Describe the morphology of the erythrocytes.
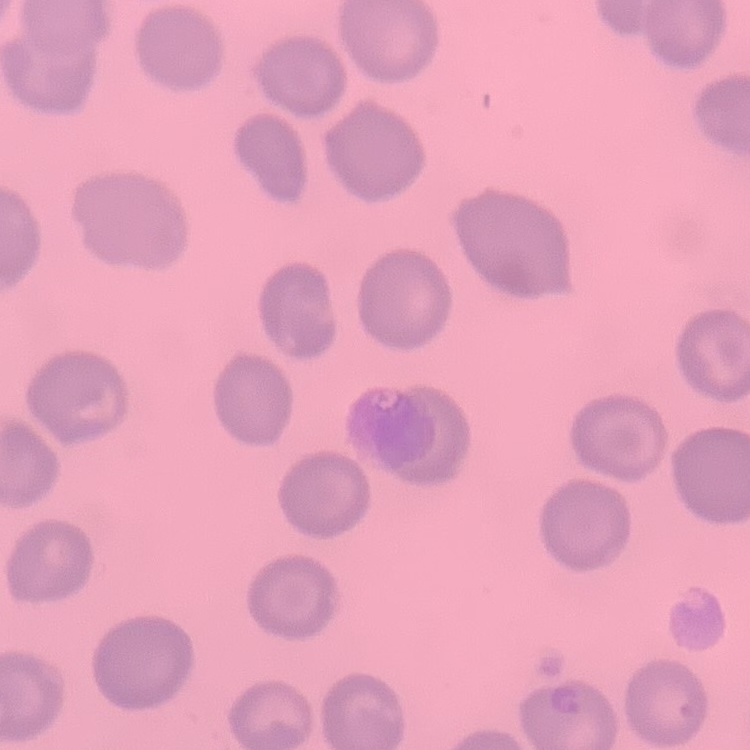

No rouleaux formation.

{
  "image_type": "square crop of a larger photomicrograph",
  "stain": "Field's or Giemsa",
  "preparation": "thin blood film"
}